Assess the morphology of the red blood cells.
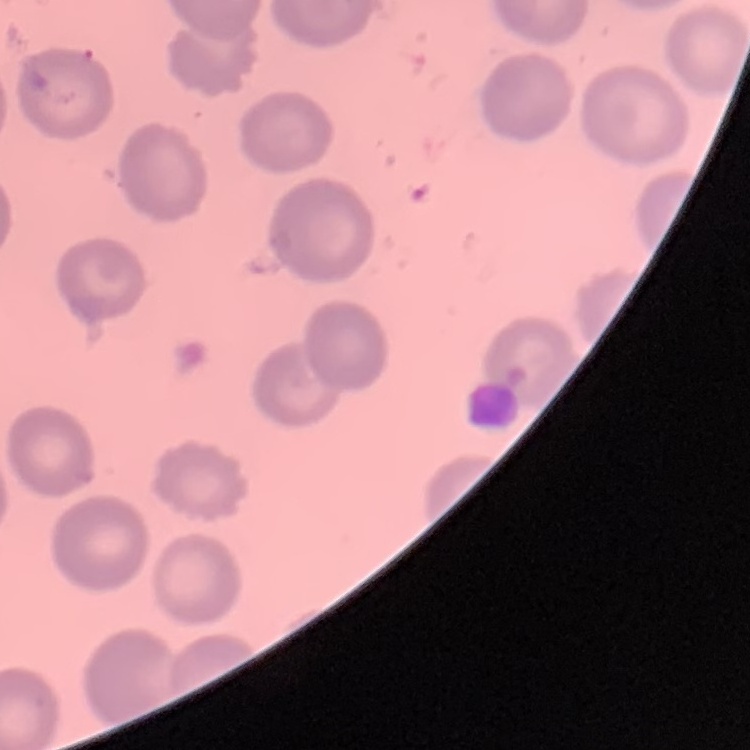
No rouleaux formation.

Summary:
  - Image type: square crop of a larger photomicrograph
  - Stain: Field's or Giemsa
  - Preparation: thin blood film